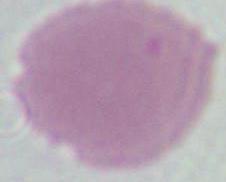

Summary:
  - Magnification: 1000x
  - Identification: red blood cell
  - Modality: micrograph